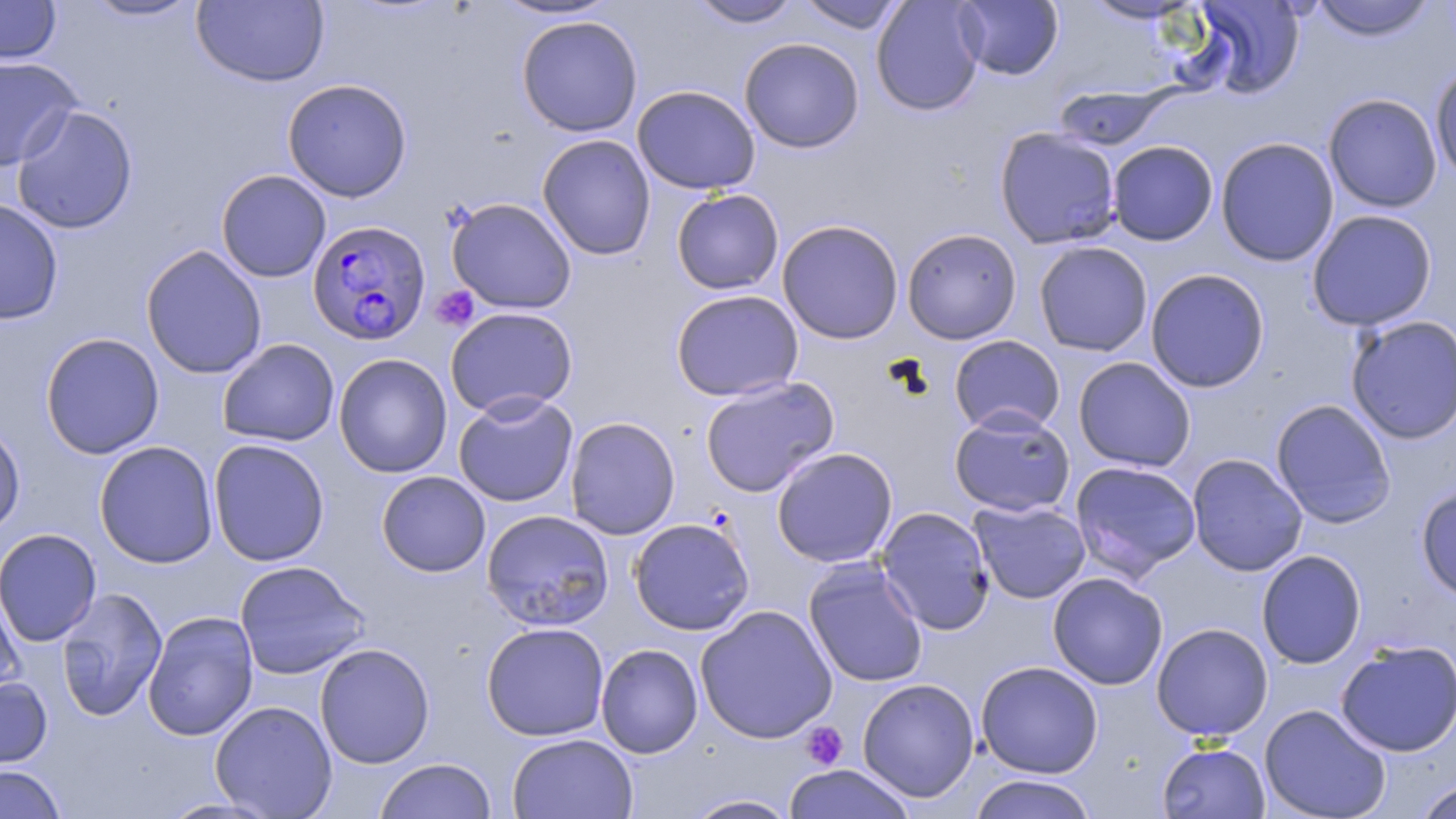 Approximate bounding boxes as (x1, y1, x2, y2) in pixels. Platelet locations: (430, 286, 480, 331), (799, 721, 848, 771). Plasmodium falciparum-infected red blood cell locations: (307, 220, 432, 345). Uninfected red blood cell locations: (0, 0, 62, 65), (82, 0, 204, 22), (192, 0, 329, 87), (491, 0, 622, 21), (688, 0, 803, 29), (795, 0, 910, 34), (871, 0, 985, 116), (953, 0, 1063, 80), (1081, 0, 1205, 25), (1192, 0, 1307, 99), (1309, 0, 1437, 42), (516, 15, 643, 137), (739, 37, 865, 154), (0, 55, 81, 171), (1429, 60, 1456, 183), (282, 78, 413, 202), (632, 85, 761, 195), (1052, 85, 1173, 150), (1323, 93, 1443, 213), (12, 104, 138, 235), (994, 127, 1123, 249), (537, 133, 656, 260), (1215, 137, 1340, 267), (1107, 140, 1219, 246), (216, 169, 331, 283), (671, 188, 784, 295), (446, 197, 577, 315), (0, 198, 64, 325), (1306, 209, 1438, 331), (777, 219, 904, 345), (901, 228, 1022, 344), (1034, 241, 1153, 357), (140, 245, 268, 379), (1145, 267, 1270, 393), (670, 289, 804, 402), (444, 306, 578, 418), (1345, 314, 1456, 444), (40, 332, 164, 459), (949, 335, 1065, 435), (217, 338, 340, 447), (333, 353, 452, 478), (1073, 357, 1195, 472), (699, 376, 840, 498), (453, 392, 578, 507), (1270, 398, 1397, 529), (948, 408, 1076, 517), (565, 416, 681, 540), (0, 418, 26, 538), (208, 438, 330, 567), (94, 440, 219, 568), (771, 446, 898, 568), (1186, 453, 1308, 576), (1069, 460, 1202, 581), (376, 470, 490, 577), (1415, 483, 1456, 603), (968, 499, 1091, 604), (875, 506, 996, 635), (481, 509, 615, 631), (628, 517, 755, 635), (1, 528, 102, 647), (1256, 550, 1366, 669), (803, 559, 929, 688), (234, 560, 370, 680), (1047, 572, 1168, 690), (0, 581, 26, 701), (55, 587, 168, 722), (695, 604, 838, 744), (142, 611, 258, 741), (481, 622, 610, 741), (1151, 622, 1273, 741), (1336, 638, 1456, 757), (314, 642, 435, 768), (596, 643, 703, 758), (975, 661, 1104, 778), (0, 676, 52, 769), (857, 678, 980, 802), (210, 700, 338, 818), (1259, 703, 1391, 819), (507, 733, 638, 819), (1157, 741, 1270, 819), (374, 758, 497, 819), (0, 764, 67, 819), (783, 764, 915, 819), (966, 774, 1100, 818), (1413, 778, 1456, 819), (683, 794, 802, 818), (159, 797, 282, 818). Slide-level diagnosis: Plasmodium falciparum. Image is 1456×819 pixels. May-Grünwald-Giemsa-stained preparation. One field of a larger specimen. Optical microscopy. Captured at 1000x magnification. Thin blood film.